Outline each blood parasite and name the species.
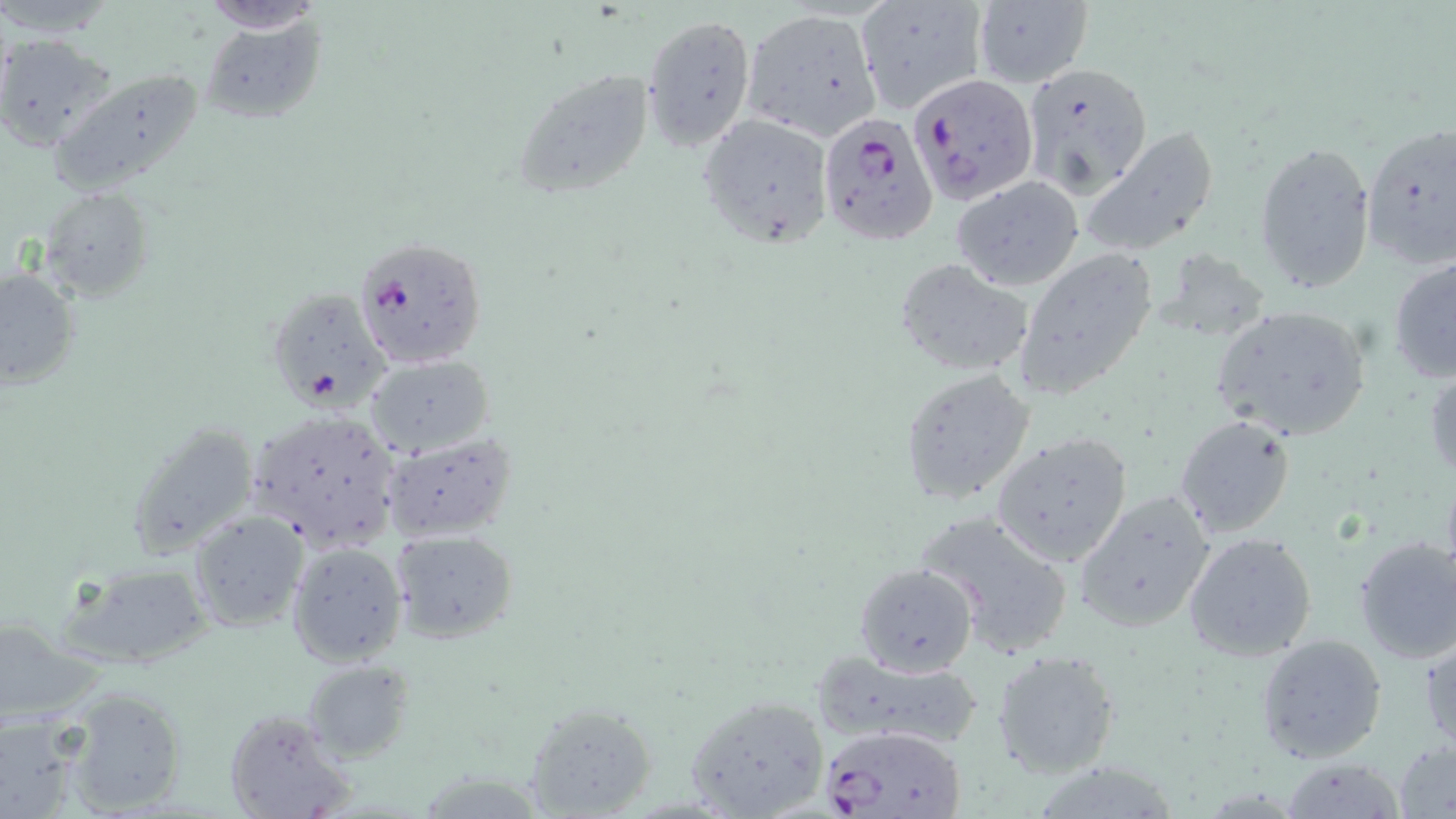

Approximate bounding boxes as [x1, y1, x2, y2] in pixels.
Plasmodium falciparum-infected red blood cells: [907, 72, 1035, 203], [816, 113, 942, 245], [356, 237, 489, 370], [820, 723, 964, 818].
No Plasmodium ovale, Plasmodium malariae, Plasmodium vivax, Babesia divergens, or Trypanosoma brucei observed.

Summary:
  - Uninfected red blood cell locations: [855, 1, 990, 115], [972, 1, 1093, 89], [201, 3, 326, 34], [741, 10, 883, 140], [642, 15, 755, 149], [198, 19, 324, 127], [3, 35, 119, 154], [1020, 62, 1149, 194], [49, 65, 207, 193], [512, 67, 656, 199], [698, 112, 833, 247], [1361, 121, 1456, 268], [1083, 129, 1220, 257], [1253, 139, 1377, 295], [950, 177, 1085, 292], [40, 187, 153, 299], [1011, 247, 1157, 401], [1149, 249, 1273, 345], [1388, 254, 1455, 384], [896, 259, 1034, 379], [0, 266, 80, 389], [266, 287, 393, 410], [1209, 304, 1372, 444], [363, 355, 494, 459], [1424, 359, 1456, 483], [899, 367, 1037, 506], [244, 410, 402, 552], [1174, 413, 1296, 540], [126, 420, 260, 562], [990, 431, 1136, 568], [379, 433, 519, 542], [1074, 489, 1219, 634], [919, 511, 1073, 657], [188, 512, 308, 633], [390, 529, 519, 644], [1183, 532, 1319, 662], [1353, 535, 1456, 666], [286, 543, 408, 666], [56, 560, 216, 669], [853, 561, 978, 677], [1420, 629, 1455, 751], [1255, 633, 1388, 763], [991, 648, 1121, 779], [809, 649, 987, 754], [300, 659, 415, 762], [59, 684, 191, 814], [681, 693, 831, 819], [523, 702, 655, 818], [225, 708, 352, 819], [0, 711, 86, 819], [1393, 737, 1456, 818], [1279, 758, 1408, 818]
  - Slide-level diagnosis: Plasmodium falciparum
  - Preparation: thin blood film
  - Modality: optical microscopy
  - Field of view: single
  - Magnification: 1000x
  - Stain: May-Grünwald-Giemsa
  - Image size: 1456×819 pixels